State which parasite is depicted.
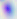

This is Toxoplasma gondii.

modality: photomicrograph
magnification: 400x